Locate every blood parasite and identify its species.
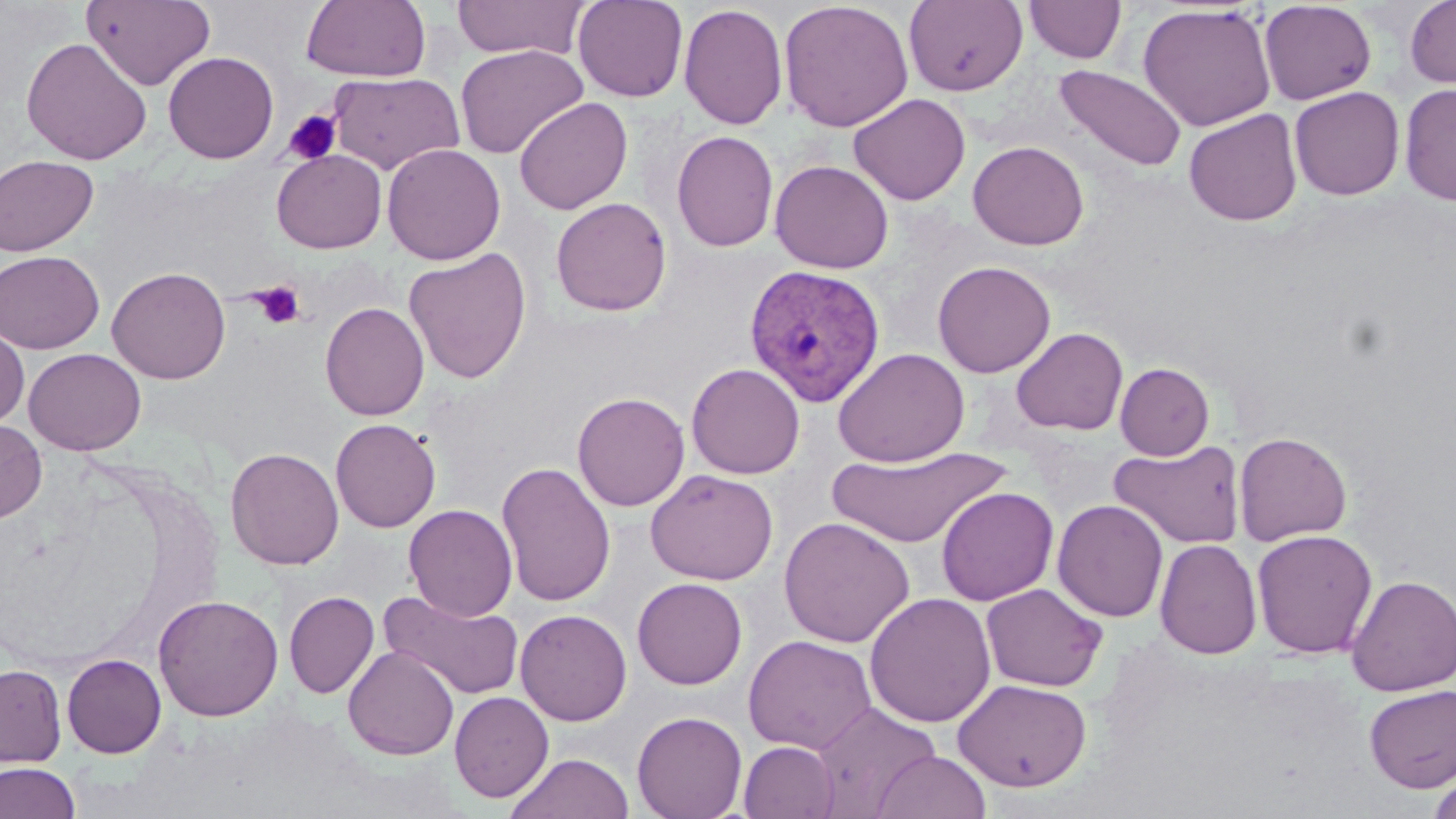

Approximate bounding boxes as (x1, y1, x2, y2) in pixels.
Plasmodium vivax-infected red blood cells: (743, 263, 886, 406).
No Plasmodium falciparum, Plasmodium ovale, Plasmodium malariae, Babesia divergens, or Trypanosoma brucei observed.

Platelet locations: (282, 109, 342, 166), (250, 281, 306, 330). Uninfected red blood cell locations: (81, 0, 215, 90), (300, 0, 431, 82), (451, 0, 590, 61), (573, 0, 688, 102), (904, 0, 1028, 96), (1024, 0, 1126, 64), (1405, 0, 1456, 90), (778, 1, 914, 132), (1259, 1, 1377, 105), (1137, 3, 1276, 131), (679, 4, 788, 130), (20, 37, 153, 165), (455, 43, 588, 159), (162, 51, 279, 164), (1054, 64, 1187, 172), (328, 71, 464, 175), (1399, 82, 1456, 206), (1289, 86, 1404, 200), (848, 93, 970, 205), (514, 96, 633, 215), (1184, 109, 1302, 226), (672, 130, 778, 252), (968, 141, 1089, 250), (382, 143, 506, 265), (271, 149, 387, 253), (0, 154, 98, 257), (770, 160, 894, 273), (551, 197, 672, 316), (403, 248, 532, 383), (0, 250, 104, 353), (932, 260, 1056, 378), (107, 266, 231, 384), (319, 301, 430, 421), (0, 325, 29, 429), (1010, 327, 1128, 435), (833, 347, 970, 468), (24, 348, 147, 455), (686, 362, 805, 479), (1115, 363, 1214, 460), (572, 391, 690, 511), (0, 417, 47, 523), (331, 419, 441, 533), (1234, 432, 1352, 545), (1109, 439, 1246, 549), (225, 447, 344, 570), (827, 447, 1010, 549), (497, 461, 616, 607), (645, 469, 779, 585), (936, 486, 1058, 606), (1052, 500, 1168, 622), (403, 504, 517, 620), (778, 516, 914, 648), (1251, 529, 1378, 658), (1154, 538, 1262, 659), (1346, 574, 1456, 696), (632, 578, 748, 689), (980, 582, 1108, 692), (378, 589, 524, 702), (284, 591, 379, 698), (865, 592, 996, 728), (153, 593, 284, 721), (515, 609, 632, 726), (743, 634, 876, 754), (343, 645, 459, 760), (62, 653, 166, 758), (0, 664, 66, 767), (952, 677, 1092, 792), (1364, 684, 1456, 792), (449, 691, 554, 802), (811, 702, 941, 816), (632, 710, 748, 819), (739, 740, 839, 818), (871, 750, 991, 818), (505, 752, 635, 819), (0, 762, 81, 819), (1427, 771, 1456, 819). Slide-level diagnosis: Plasmodium vivax. Captured at 1000x magnification. Thin blood smear. Single field of view. Image is 1456×819 pixels. Optical microscopy. May-Grünwald-Giemsa-stained preparation.